Assess this cell for malaria.
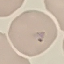
It is parasitized.

preparation = thin smear
image type = automatically extracted cell patch, resized to 64 × 64 pixels
stain = Giemsa
capture = smartphone through the microscope eyepiece